Describe the morphology of the red blood cells.
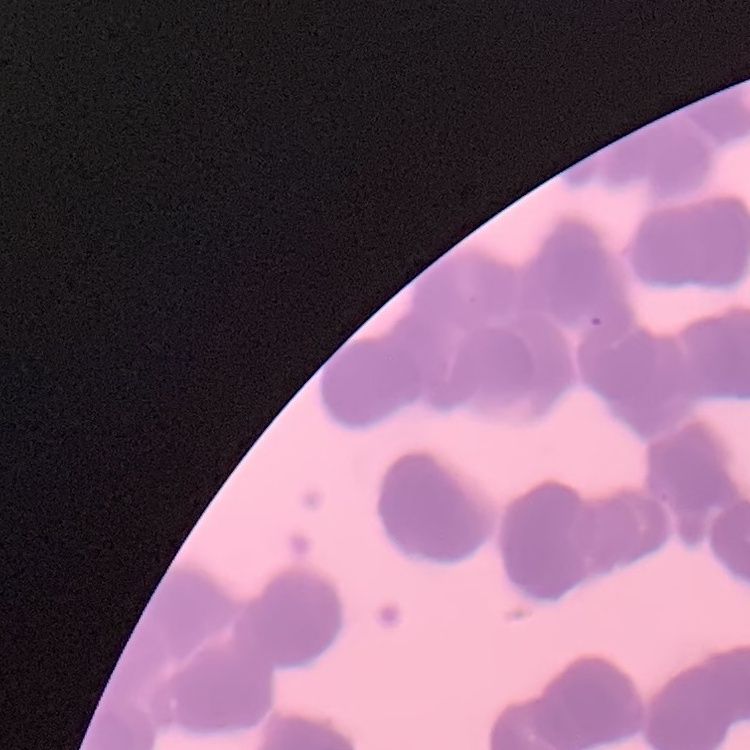
Rouleaux formation.

preparation = thin blood smear
stain = Field's or Giemsa
image type = one tile cut from a larger photomicrograph